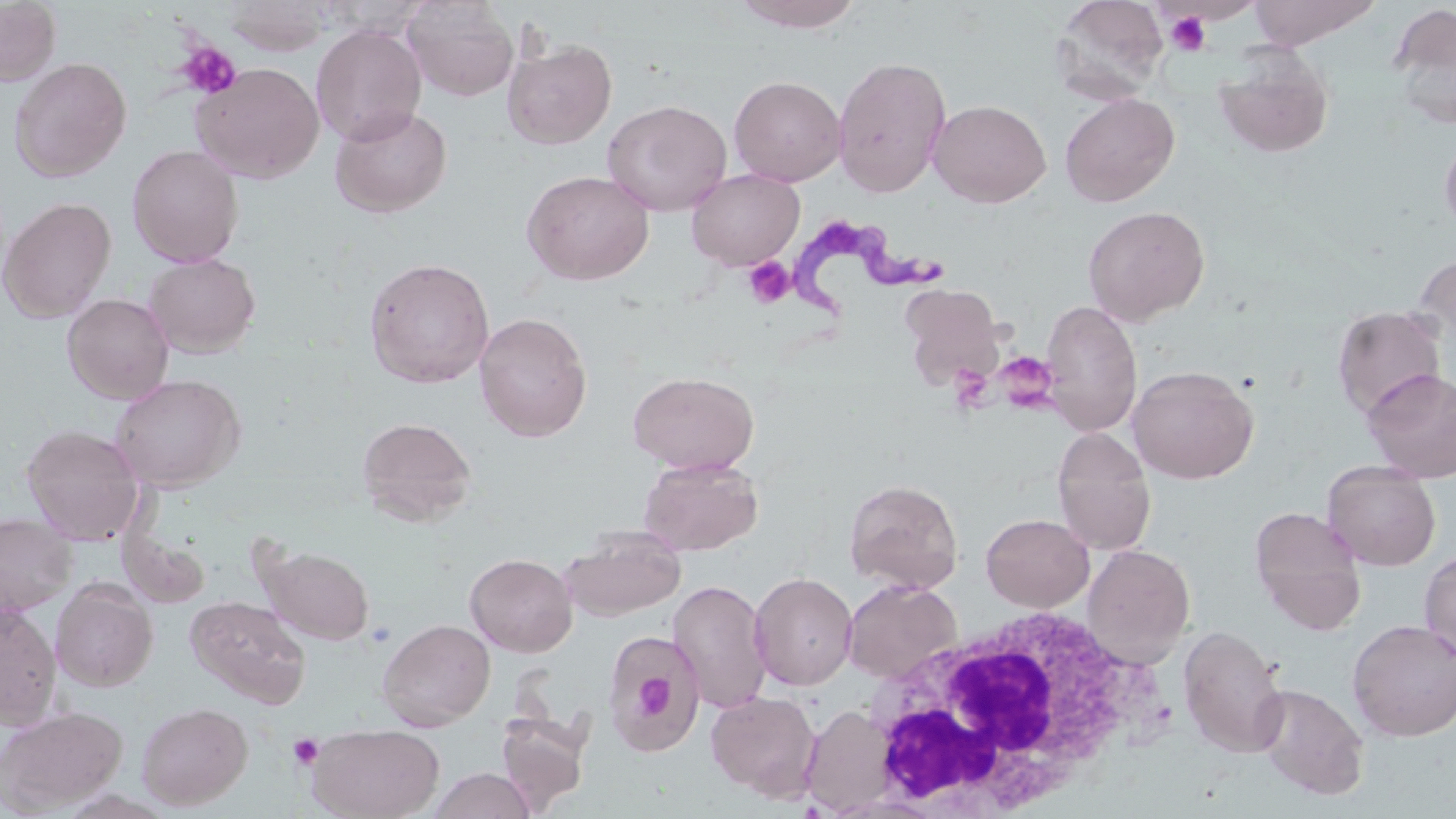

slide-level diagnosis = Trypanosoma brucei
magnification = 1000x
stain = May-Grünwald-Giemsa
modality = light microscopy
white blood cell locations = approximate bounding boxes as named x1/y1/x2/y2 corners in pixels: (x1=856, y1=603, x2=1171, y2=819)
field of view = single
Trypanosoma brucei locations = approximate bounding boxes as named x1/y1/x2/y2 corners in pixels: (x1=788, y1=216, x2=948, y2=318)
platelet locations = approximate bounding boxes as named x1/y1/x2/y2 corners in pixels: (x1=1164, y1=11, x2=1212, y2=55), (x1=177, y1=41, x2=241, y2=99), (x1=742, y1=257, x2=794, y2=309), (x1=1005, y1=356, x2=1059, y2=420), (x1=945, y1=366, x2=1000, y2=414), (x1=629, y1=666, x2=675, y2=726), (x1=288, y1=734, x2=324, y2=771)
uninfected red blood cell locations = approximate bounding boxes as named x1/y1/x2/y2 corners in pixels: (x1=733, y1=0, x2=865, y2=32), (x1=1050, y1=0, x2=1170, y2=103), (x1=1248, y1=0, x2=1379, y2=48), (x1=0, y1=1, x2=61, y2=86), (x1=223, y1=1, x2=332, y2=56), (x1=404, y1=1, x2=518, y2=101), (x1=1388, y1=4, x2=1456, y2=127), (x1=311, y1=23, x2=427, y2=146), (x1=503, y1=38, x2=617, y2=149), (x1=1214, y1=51, x2=1334, y2=159), (x1=832, y1=55, x2=952, y2=198), (x1=9, y1=57, x2=131, y2=182), (x1=190, y1=62, x2=325, y2=184), (x1=729, y1=75, x2=847, y2=186), (x1=1059, y1=92, x2=1180, y2=207), (x1=602, y1=99, x2=732, y2=216), (x1=929, y1=99, x2=1051, y2=208), (x1=330, y1=104, x2=453, y2=218), (x1=1440, y1=132, x2=1456, y2=235), (x1=127, y1=144, x2=245, y2=268), (x1=686, y1=168, x2=805, y2=271), (x1=521, y1=170, x2=654, y2=285), (x1=0, y1=197, x2=117, y2=323), (x1=1083, y1=205, x2=1210, y2=326), (x1=143, y1=253, x2=261, y2=358), (x1=1409, y1=254, x2=1456, y2=367), (x1=364, y1=257, x2=495, y2=388), (x1=899, y1=285, x2=1003, y2=387), (x1=62, y1=293, x2=174, y2=403), (x1=1040, y1=300, x2=1142, y2=436), (x1=1330, y1=306, x2=1448, y2=419), (x1=474, y1=311, x2=592, y2=443), (x1=1128, y1=365, x2=1258, y2=484), (x1=1361, y1=368, x2=1456, y2=483), (x1=627, y1=371, x2=760, y2=474), (x1=109, y1=373, x2=246, y2=492), (x1=356, y1=416, x2=478, y2=526), (x1=21, y1=424, x2=147, y2=545), (x1=1051, y1=427, x2=1156, y2=555), (x1=639, y1=456, x2=763, y2=556), (x1=1322, y1=460, x2=1441, y2=571), (x1=844, y1=479, x2=963, y2=594), (x1=1249, y1=507, x2=1366, y2=633), (x1=0, y1=513, x2=76, y2=615), (x1=980, y1=514, x2=1094, y2=612), (x1=118, y1=524, x2=212, y2=610), (x1=564, y1=526, x2=685, y2=619), (x1=1083, y1=544, x2=1196, y2=668), (x1=263, y1=546, x2=374, y2=644), (x1=1420, y1=549, x2=1456, y2=664), (x1=465, y1=552, x2=577, y2=657), (x1=749, y1=572, x2=858, y2=690), (x1=51, y1=579, x2=157, y2=691), (x1=668, y1=579, x2=772, y2=714), (x1=842, y1=579, x2=962, y2=683), (x1=185, y1=595, x2=311, y2=709), (x1=0, y1=604, x2=61, y2=728), (x1=376, y1=618, x2=495, y2=731), (x1=1347, y1=619, x2=1456, y2=741), (x1=1178, y1=625, x2=1289, y2=757), (x1=603, y1=629, x2=707, y2=753), (x1=1254, y1=683, x2=1369, y2=800), (x1=706, y1=690, x2=821, y2=801), (x1=137, y1=702, x2=253, y2=810), (x1=0, y1=705, x2=127, y2=816), (x1=801, y1=705, x2=898, y2=814), (x1=496, y1=713, x2=591, y2=813), (x1=308, y1=723, x2=445, y2=819), (x1=426, y1=767, x2=536, y2=819)
image size = 1456×819 pixels
preparation = thin blood smear